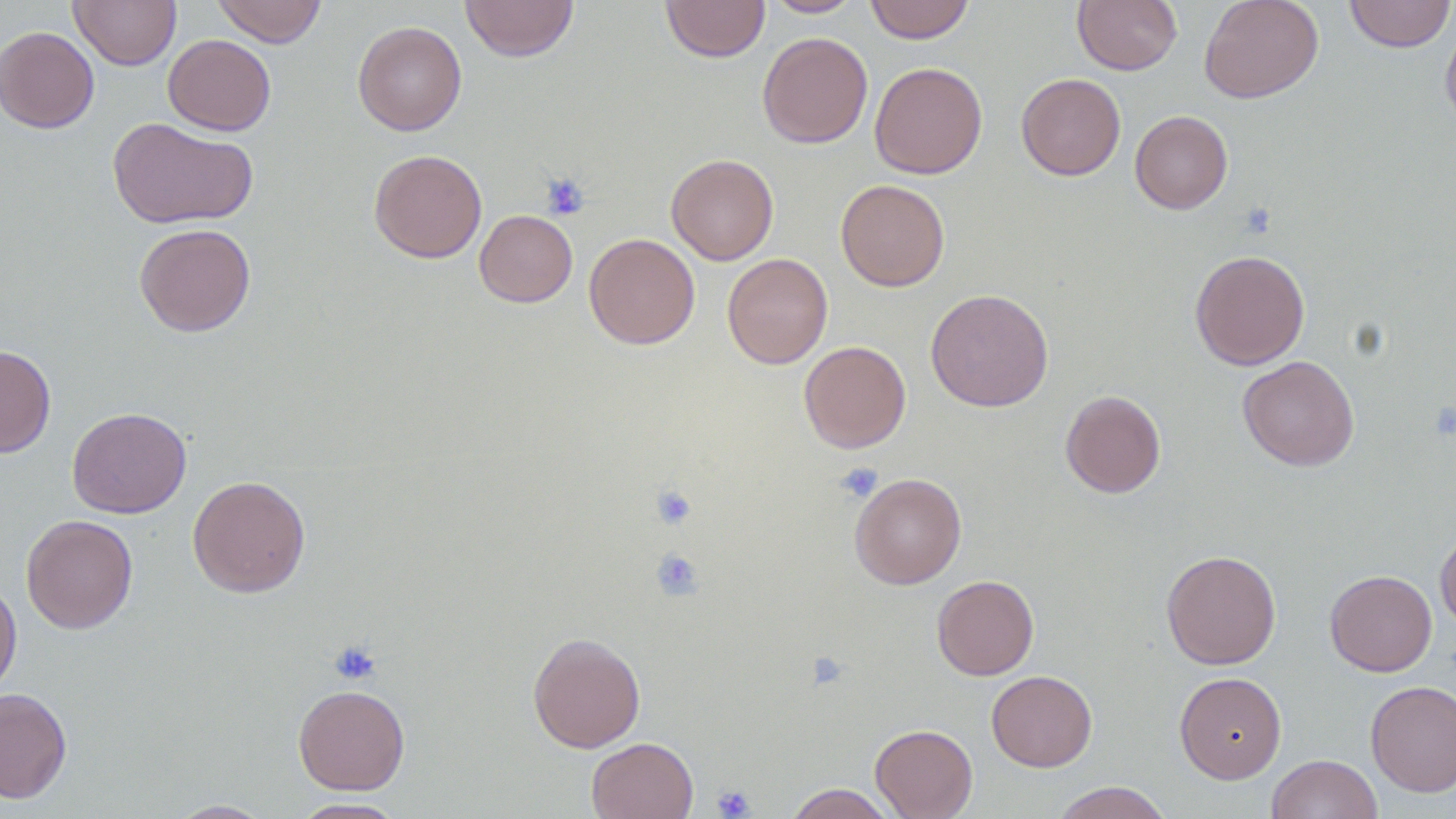
slide-level diagnosis = no evidence of blood parasites
preparation = thin blood film
modality = optical microscopy
magnification = 1000x
field of view = one of a larger specimen
platelet locations = approximate bounding boxes as [x1, y1, x2, y2] in pixels: [540, 172, 589, 220], [835, 463, 883, 503], [650, 484, 698, 530], [650, 548, 704, 601], [328, 642, 382, 686], [807, 652, 848, 690], [712, 785, 755, 818]
image size = 1456×819 pixels
uninfected red blood cell locations = approximate bounding boxes as [x1, y1, x2, y2] in pixels: [70, 0, 181, 70], [212, 0, 327, 47], [461, 0, 578, 62], [660, 0, 770, 62], [762, 0, 865, 17], [864, 0, 975, 44], [1072, 0, 1182, 74], [1198, 0, 1324, 104], [1343, 0, 1455, 52], [1440, 19, 1456, 136], [352, 20, 466, 136], [0, 26, 99, 133], [757, 31, 873, 149], [163, 34, 276, 136], [869, 61, 987, 179], [1016, 73, 1125, 181], [1130, 110, 1233, 214], [107, 117, 258, 228], [369, 149, 487, 263], [666, 153, 778, 265], [835, 179, 950, 292], [474, 210, 578, 307], [134, 223, 256, 337], [584, 232, 700, 350], [1189, 249, 1310, 370], [722, 252, 832, 369], [925, 288, 1054, 412], [798, 341, 911, 453], [0, 345, 56, 458], [1238, 355, 1359, 471], [1060, 390, 1166, 498], [67, 407, 191, 518], [849, 472, 966, 589], [187, 475, 311, 598], [21, 514, 138, 634], [1435, 526, 1456, 631], [1161, 549, 1281, 669], [1324, 570, 1437, 676], [932, 575, 1039, 680], [0, 577, 22, 698], [528, 632, 646, 752], [986, 670, 1097, 772], [1174, 672, 1287, 783], [1365, 680, 1456, 797], [293, 684, 410, 795], [0, 687, 72, 804], [870, 723, 978, 819], [586, 737, 699, 819], [1267, 754, 1383, 819], [1050, 782, 1174, 819], [784, 783, 896, 818], [290, 797, 407, 818], [166, 799, 275, 818]